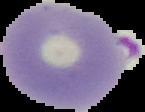
preparation = thin blood film
image size = 145×112 pixels
image type = segmented cell region on a black background
malaria status = parasitized